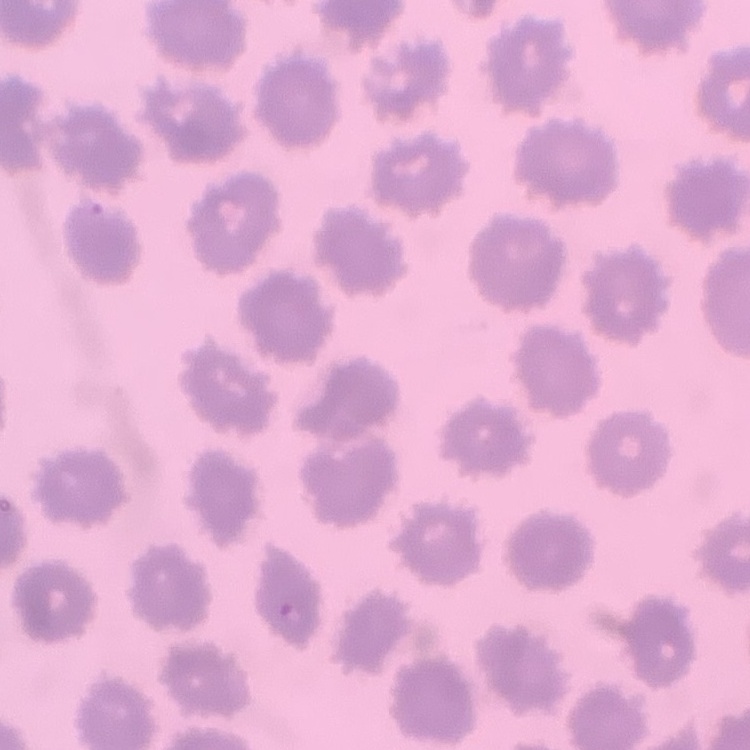

Summary:
  - Red blood cell morphology: no rouleaux formation
  - Preparation: thin blood film
  - Stain: Field's or Giemsa
  - Image type: one tile cut from a larger photomicrograph